Classify this cell by malaria status.
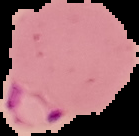

It is parasitized.

Summary:
  - Image size: 139×136 pixels
  - Preparation: thin blood film
  - Image type: cell region segmented out of the field of view; surrounding area masked to black